Locate every Plasmodium malariae-infected red blood cell.
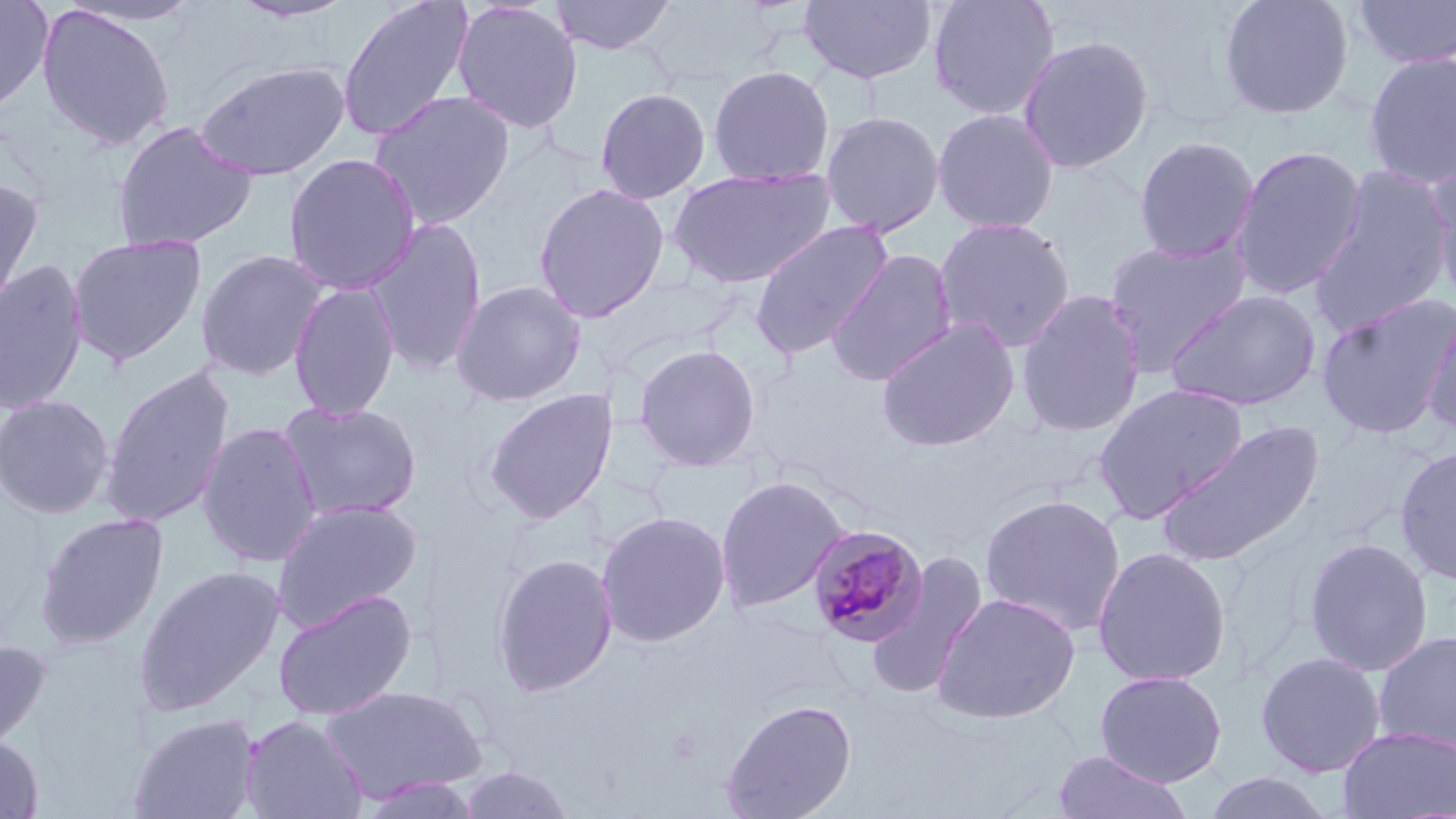
Approximate bounding boxes as named x1/y1/x2/y2 corners in pixels.
Plasmodium malariae-infected red blood cells: (x1=805, y1=525, x2=929, y2=649).

Uninfected red blood cell locations: (x1=0, y1=0, x2=53, y2=115), (x1=60, y1=0, x2=206, y2=27), (x1=228, y1=0, x2=359, y2=23), (x1=336, y1=0, x2=475, y2=143), (x1=548, y1=0, x2=678, y2=56), (x1=799, y1=0, x2=938, y2=85), (x1=927, y1=0, x2=1059, y2=121), (x1=1219, y1=0, x2=1355, y2=120), (x1=451, y1=1, x2=584, y2=134), (x1=1350, y1=1, x2=1456, y2=69), (x1=36, y1=3, x2=176, y2=150), (x1=1017, y1=34, x2=1155, y2=174), (x1=1363, y1=51, x2=1456, y2=190), (x1=195, y1=60, x2=350, y2=182), (x1=708, y1=65, x2=835, y2=187), (x1=594, y1=88, x2=711, y2=204), (x1=367, y1=89, x2=516, y2=229), (x1=932, y1=108, x2=1060, y2=235), (x1=820, y1=110, x2=945, y2=237), (x1=110, y1=121, x2=259, y2=253), (x1=1134, y1=136, x2=1259, y2=262), (x1=1231, y1=145, x2=1367, y2=300), (x1=282, y1=153, x2=420, y2=295), (x1=1427, y1=163, x2=1456, y2=309), (x1=667, y1=167, x2=837, y2=288), (x1=1309, y1=167, x2=1454, y2=337), (x1=0, y1=176, x2=42, y2=329), (x1=532, y1=182, x2=670, y2=323), (x1=364, y1=217, x2=488, y2=376), (x1=933, y1=217, x2=1076, y2=352), (x1=749, y1=219, x2=892, y2=360), (x1=68, y1=233, x2=208, y2=367), (x1=1104, y1=235, x2=1251, y2=370), (x1=825, y1=249, x2=958, y2=386), (x1=196, y1=250, x2=329, y2=381), (x1=0, y1=258, x2=89, y2=417), (x1=450, y1=280, x2=587, y2=407), (x1=288, y1=282, x2=400, y2=421), (x1=1165, y1=289, x2=1321, y2=412), (x1=1016, y1=290, x2=1146, y2=438), (x1=1315, y1=294, x2=1456, y2=440), (x1=1421, y1=304, x2=1456, y2=439), (x1=876, y1=316, x2=1021, y2=453), (x1=634, y1=344, x2=761, y2=472), (x1=100, y1=365, x2=235, y2=530), (x1=1092, y1=383, x2=1249, y2=522), (x1=481, y1=388, x2=618, y2=524), (x1=0, y1=394, x2=115, y2=519), (x1=279, y1=400, x2=423, y2=522), (x1=1156, y1=420, x2=1324, y2=568), (x1=196, y1=421, x2=322, y2=568), (x1=1395, y1=446, x2=1456, y2=585), (x1=714, y1=475, x2=850, y2=614), (x1=980, y1=493, x2=1126, y2=637), (x1=271, y1=498, x2=424, y2=631), (x1=596, y1=511, x2=732, y2=647), (x1=35, y1=512, x2=169, y2=650), (x1=1303, y1=538, x2=1433, y2=676), (x1=1092, y1=546, x2=1232, y2=688), (x1=866, y1=551, x2=989, y2=699), (x1=491, y1=552, x2=619, y2=697), (x1=134, y1=565, x2=285, y2=716), (x1=272, y1=588, x2=418, y2=722), (x1=933, y1=593, x2=1080, y2=724), (x1=1372, y1=628, x2=1455, y2=758), (x1=0, y1=639, x2=51, y2=756), (x1=1256, y1=652, x2=1386, y2=778), (x1=1094, y1=670, x2=1227, y2=787), (x1=321, y1=685, x2=486, y2=804), (x1=720, y1=697, x2=858, y2=819), (x1=127, y1=712, x2=261, y2=819), (x1=240, y1=714, x2=368, y2=819), (x1=1338, y1=726, x2=1456, y2=819), (x1=0, y1=735, x2=43, y2=818), (x1=1052, y1=750, x2=1192, y2=819), (x1=457, y1=766, x2=577, y2=819), (x1=1201, y1=772, x2=1335, y2=818), (x1=357, y1=775, x2=484, y2=819). Slide-level diagnosis: Plasmodium malariae. Thin blood smear. Light microscopy. Single field of view. 1000x magnification. May-Grünwald-Giemsa stain. Image is 1456×819 pixels.